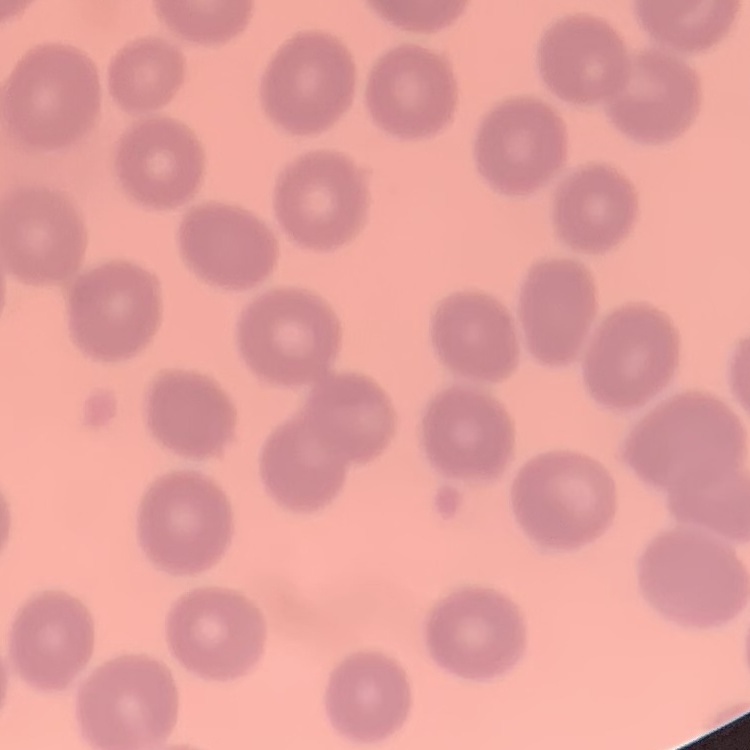
red blood cell morphology = no rouleaux formation
preparation = thin blood film
image type = one tile cut from a larger photomicrograph
stain = Field's or Giemsa